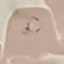
Summary:
  - Malaria status: parasitized
  - Stain: Giemsa
  - Image type: cell patch, automatically extracted from a larger field of view and resized to 64 × 64 pixels
  - Preparation: thin blood smear
  - Capture: smartphone through the microscope eyepiece